Report the malaria status of this cell.
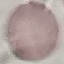

It is uninfected.

stain: Giemsa
capture: smartphone through the microscope eyepiece
preparation: thin blood film
image_type: cell patch, automatically extracted from a larger field of view and resized to 64 × 64 pixels